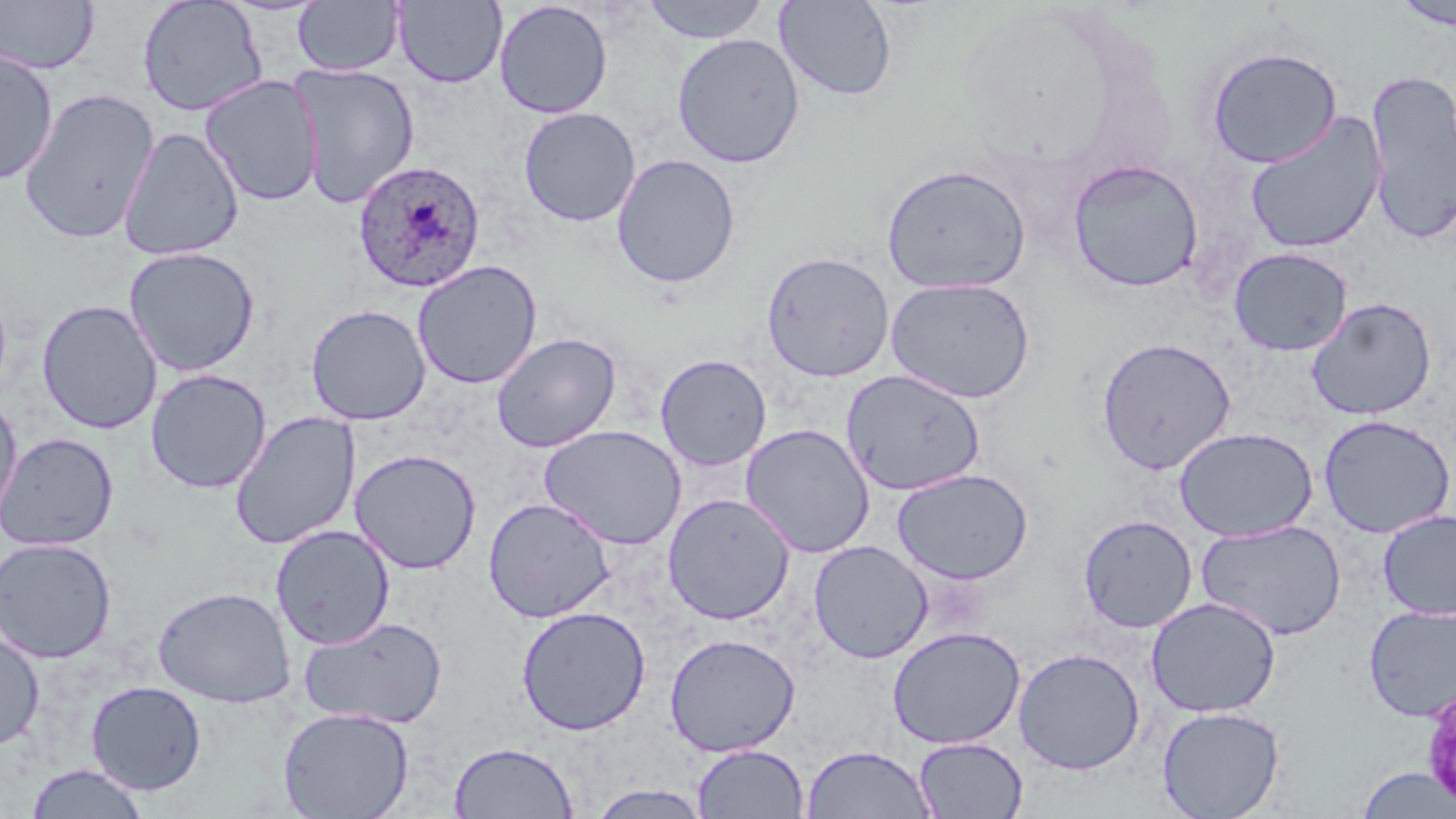

{
  "slide_level_diagnosis": "Plasmodium ovale",
  "preparation": "thin blood smear",
  "magnification": "1000x",
  "stain": "May-Grünwald-Giemsa",
  "image_size": "1456×819 pixels",
  "uninfected_red_blood_cell_locations_subset": "approximate bounding boxes as (x1,y1)-(x2,y2) corner pairs in pixels: (0,0)-(99,75), (137,0)-(268,117), (640,0)-(772,44), (774,0)-(897,101), (1390,0)-(1455,33), (293,1)-(404,77), (392,1)-(508,88), (493,1)-(613,119), (671,32)-(805,168), (1205,46)-(1343,168), (0,49)-(59,185), (1364,68)-(1456,247), (199,74)-(324,206), (19,88)-(158,244), (518,107)-(640,227), (1244,112)-(1386,255), (117,127)-(245,261), (611,153)-(741,288), (1067,158)-(1205,293), (880,163)-(1032,295), (123,246)-(261,377), (1228,247)-(1353,356), (761,252)-(895,382), (412,260)-(542,389), (884,277)-(1037,404), (1305,297)-(1437,420), (37,299)-(162,435), (306,304)-(431,425), (491,332)-(621,453), (1095,336)-(1237,475), (655,353)-(772,471), (146,369)-(272,494), (841,369)-(986,496), (0,395)-(23,520), (230,411)-(361,549), (1318,414)-(1455,538), (740,423)-(875,558), (539,424)-(687,550), (1174,427)-(1319,542), (1,432)-(118,552), (350,449)-(482,574), (891,468)-(1034,585), (661,492)-(796,625), (483,497)-(616,623), (1377,509)-(1456,620), (1078,515)-(1198,633), (1195,519)-(1347,641), (270,524)-(395,649), (0,537)-(117,663), (808,540)-(933,663), (153,585)-(296,708), (1146,597)-(1280,718), (1364,604)-(1456,722), (515,605)-(652,735), (298,615)-(449,730), (0,626)-(44,752), (887,626)-(1026,749), (664,633)-(800,757), (1013,647)-(1145,774), (85,680)-(206,795), (277,706)-(415,819), (1157,706)-(1285,819), (914,737)-(1028,818), (449,741)-(578,818), (692,743)-(809,818), (801,745)-(936,819), (26,764)-(150,819), (1356,767)-(1455,819), (586,784)-(715,818)",
  "field_of_view": "single",
  "modality": "optical microscopy",
  "plasmodium_ovale_infected_red_blood_cell_locations_subset": "approximate bounding boxes as (x1,y1)-(x2,y2) corner pairs in pixels: (352,160)-(486,293)"
}